Report the malaria status.
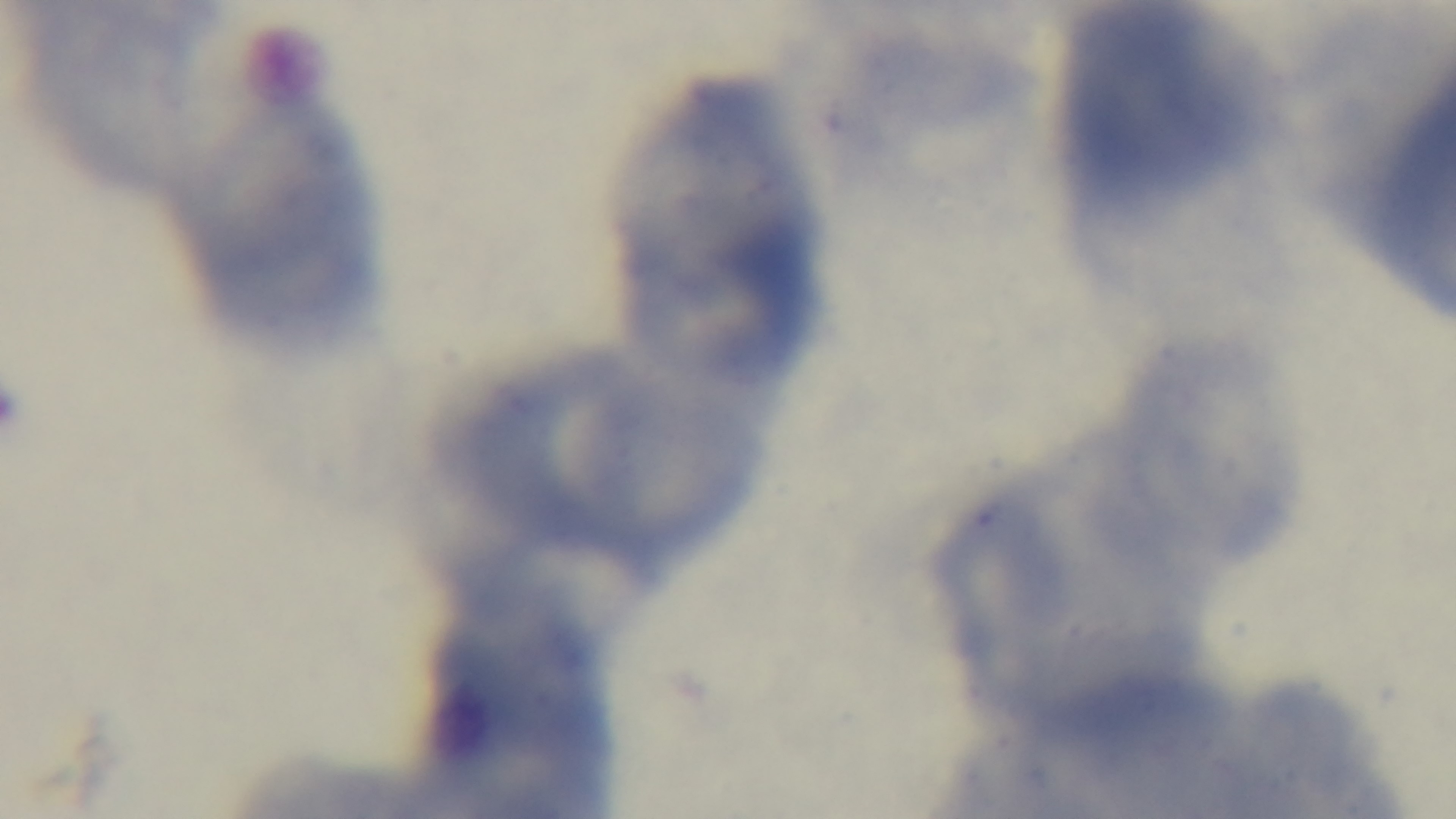

Negative.

Summary:
  - Modality: light microscopy
  - Capture: mounted 4K digital camera
  - Stain: Giemsa
  - Field of view: one from the slide
  - Preparation: thin smear
  - Objective: 100x oil immersion